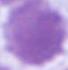
A red blood cell is seen. 1000x magnification. Micrograph.